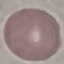
Summary:
  - Result: no malaria parasites seen
  - Image type: automatically extracted cell patch, resized to 64 × 64 pixels
  - Stain: Giemsa
  - Capture: smartphone camera at the microscope eyepiece
  - Preparation: thin smear